State the preparation type.
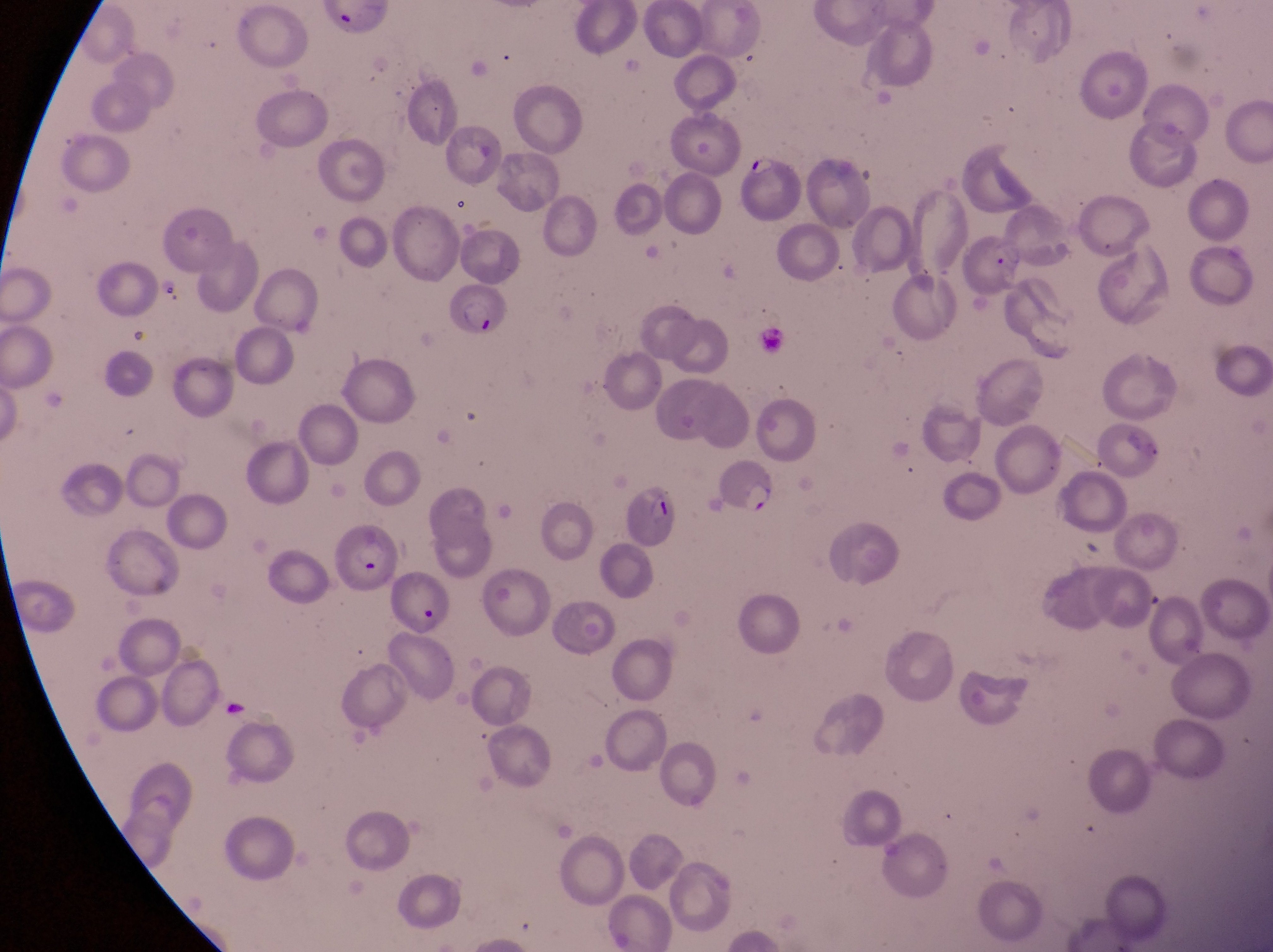
Thin blood smear.

Approximate bounding boxes as [left, top, right, bottom] in pixels.
Summary:
  - Trophozoite locations: [153, 270, 186, 309]
  - Parasitised red blood cell locations: [746, 145, 804, 222], [442, 280, 512, 337], [702, 450, 779, 518], [617, 480, 682, 550], [332, 527, 397, 589], [387, 565, 450, 632]
  - Capture: smartphone photograph through the eyepiece of an Olympus CX-23 microscope
  - Image size: 1273×952 pixels
  - Field of view: single
  - Magnification: 1000x
  - Country: Uganda